Describe the morphology of the red blood cells.
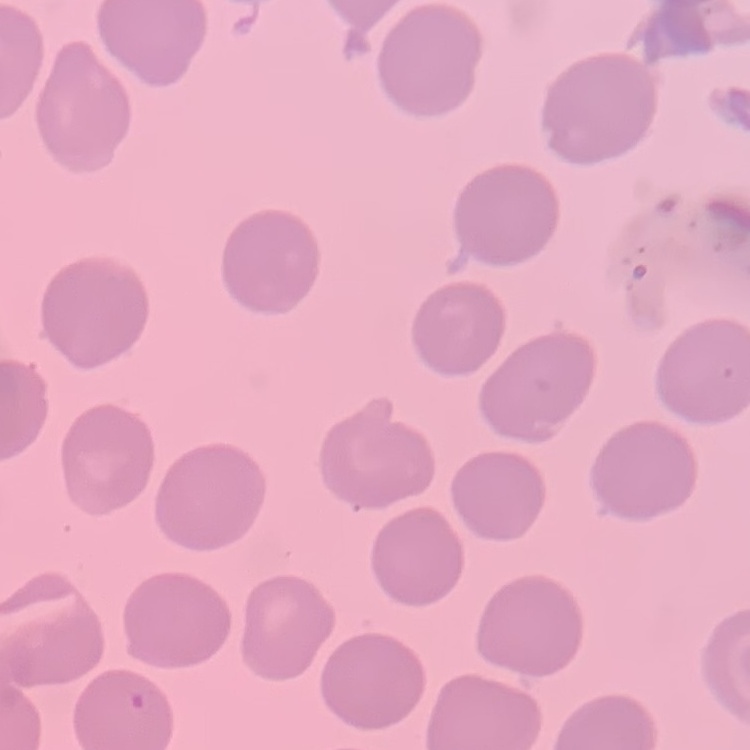
No rouleaux formation.

Square crop of a larger photomicrograph. Stained with either Field's or Giemsa. Thin blood smear.